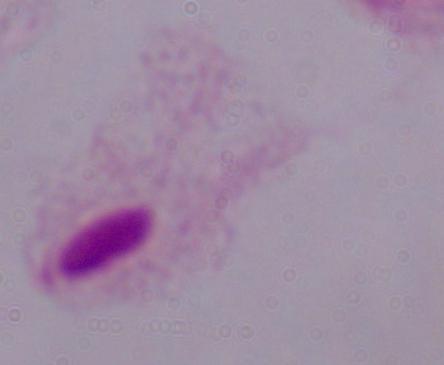

Summary:
  - Modality: photomicrograph
  - Identification: trichomonad
  - Magnification: 1000x